Report the malaria status of this cell.
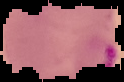
It is parasitized.

image size = 124×82 pixels
preparation = thin blood film
image type = segmented cell region on a black background